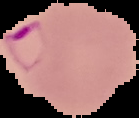

Summary:
  - Malaria status: parasitized
  - Image size: 139×118 pixels
  - Preparation: thin blood film
  - Image type: cell region segmented out of the field of view; surrounding area masked to black